Assess for Plasmodium parasites.
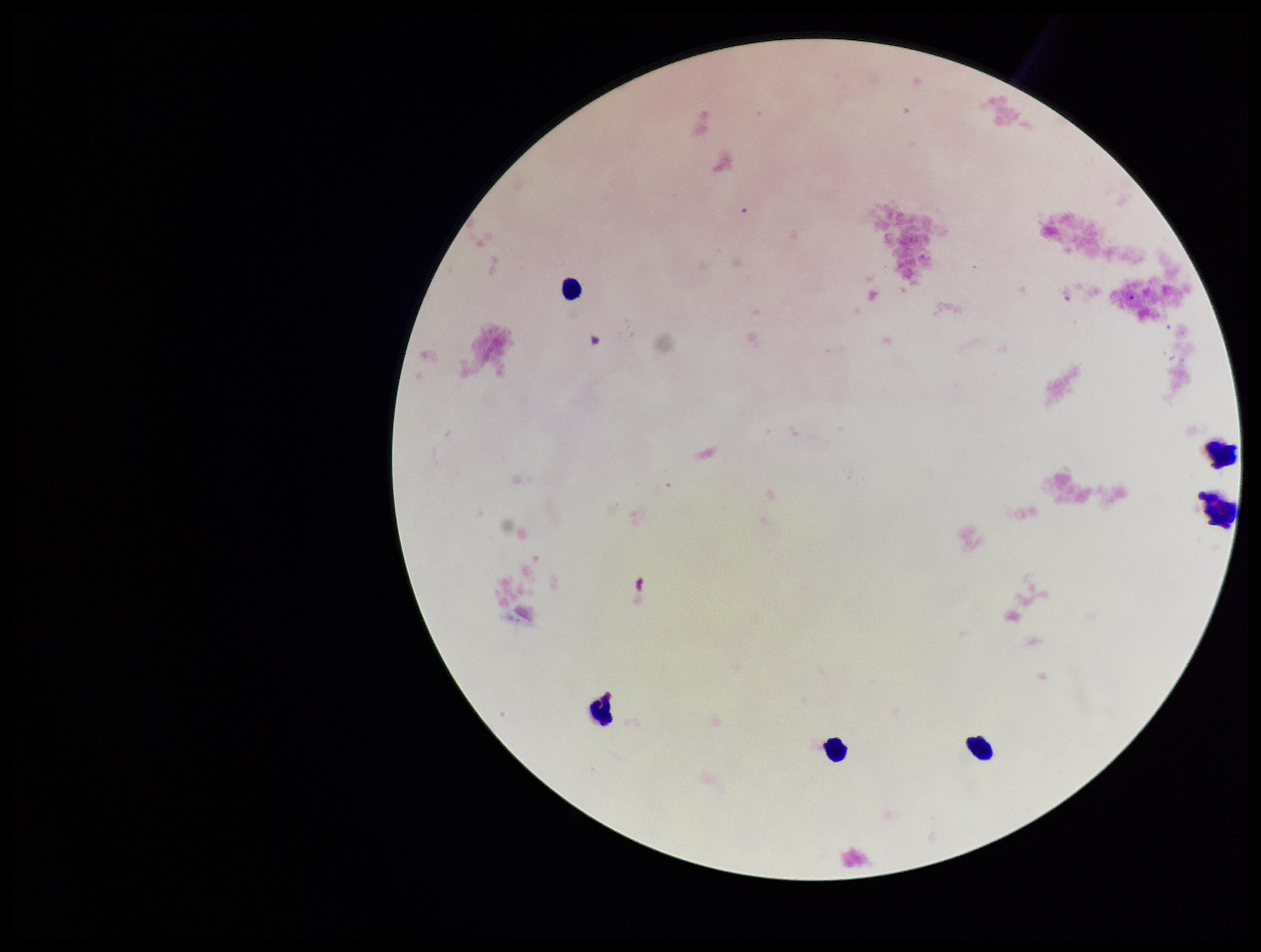
None detected.

One field from this slide. Parasite count: 0. Giemsa stain. Preparation: thick smear. Image is 1261×952 pixels. Patient malaria status: negative. Photographed through the microscope eyepiece with a smartphone camera. Leukocyte count: 6.